Assess for Plasmodium parasites.
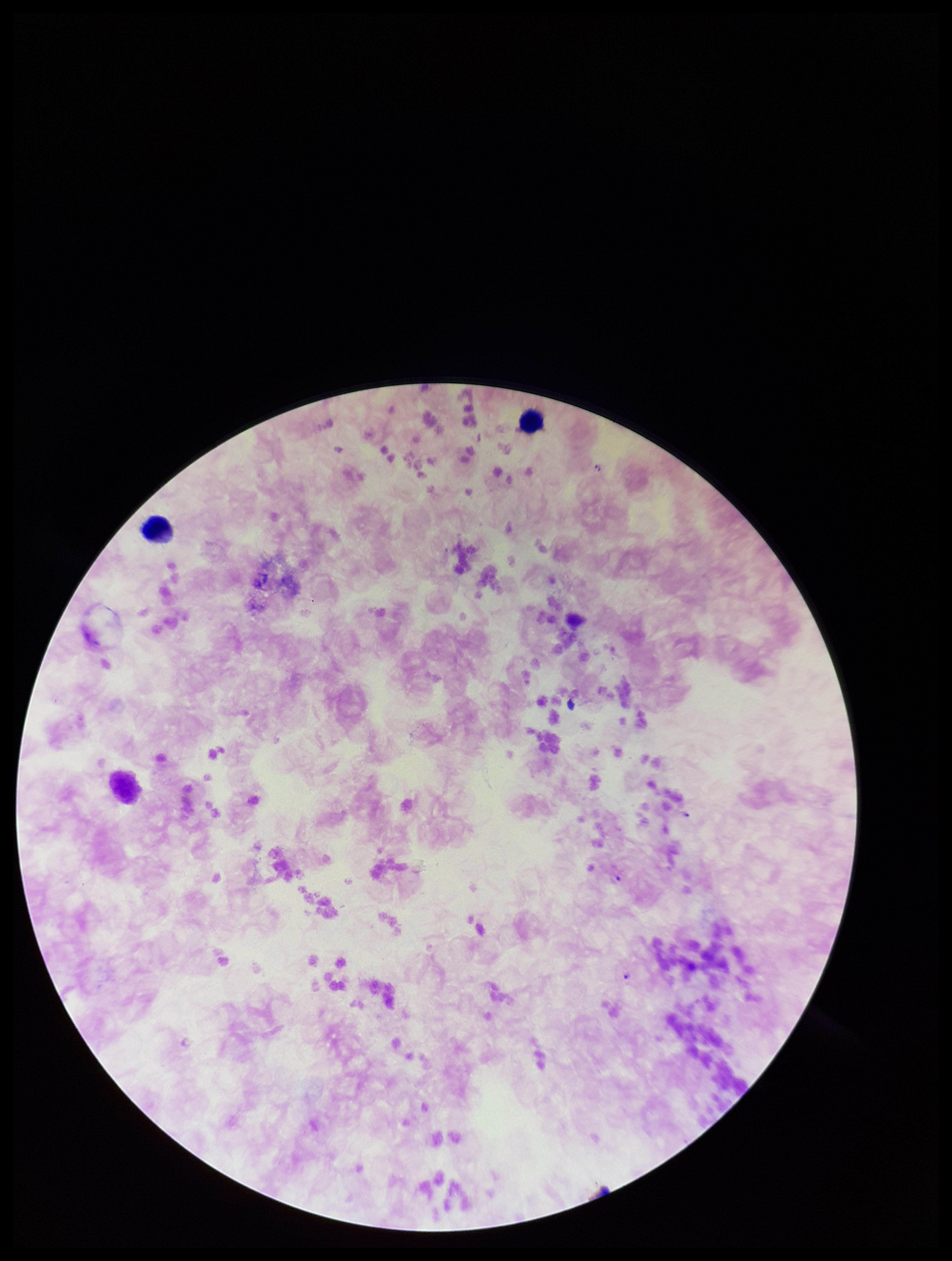

None seen.

Leukocyte count: 2. Giemsa stain. Patient malaria status: positive. Species reported for this patient: Plasmodium falciparum. Preparation: thick smear. Image is 952×1261 pixels. One field from this slide. Parasite count: 0. Photographed through the microscope eyepiece with a smartphone camera.